Name the parasite shown.
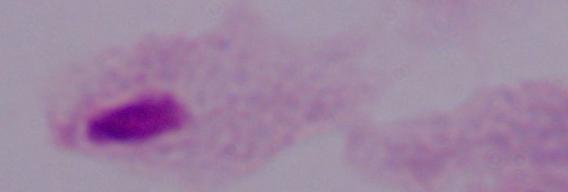
A trichomonad.

Captured at 1000x magnification. Micrograph.